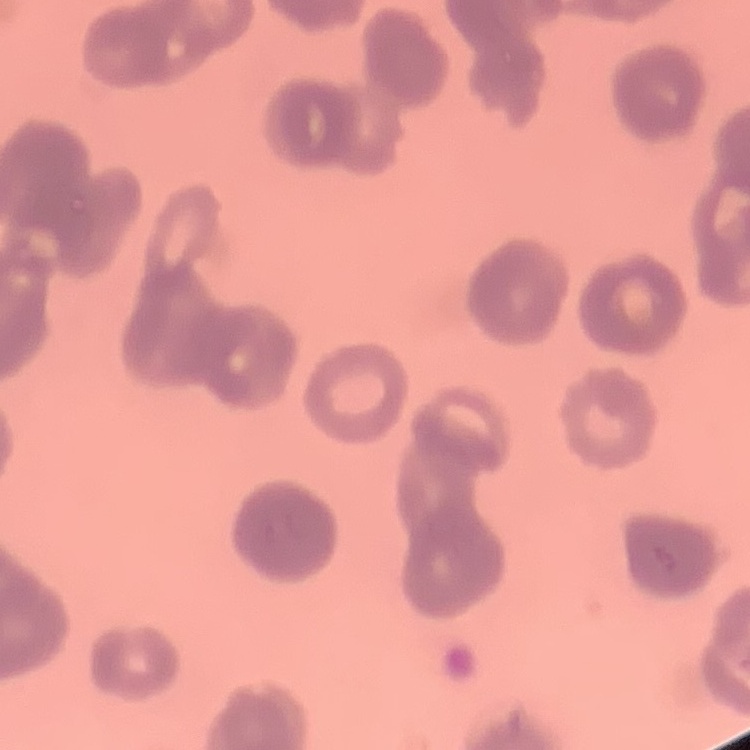
Summary:
  - Erythrocyte morphology: rouleaux formation
  - Preparation: thin peripheral smear
  - Image type: one tile cut from a larger photomicrograph
  - Stain: Field's or Giemsa